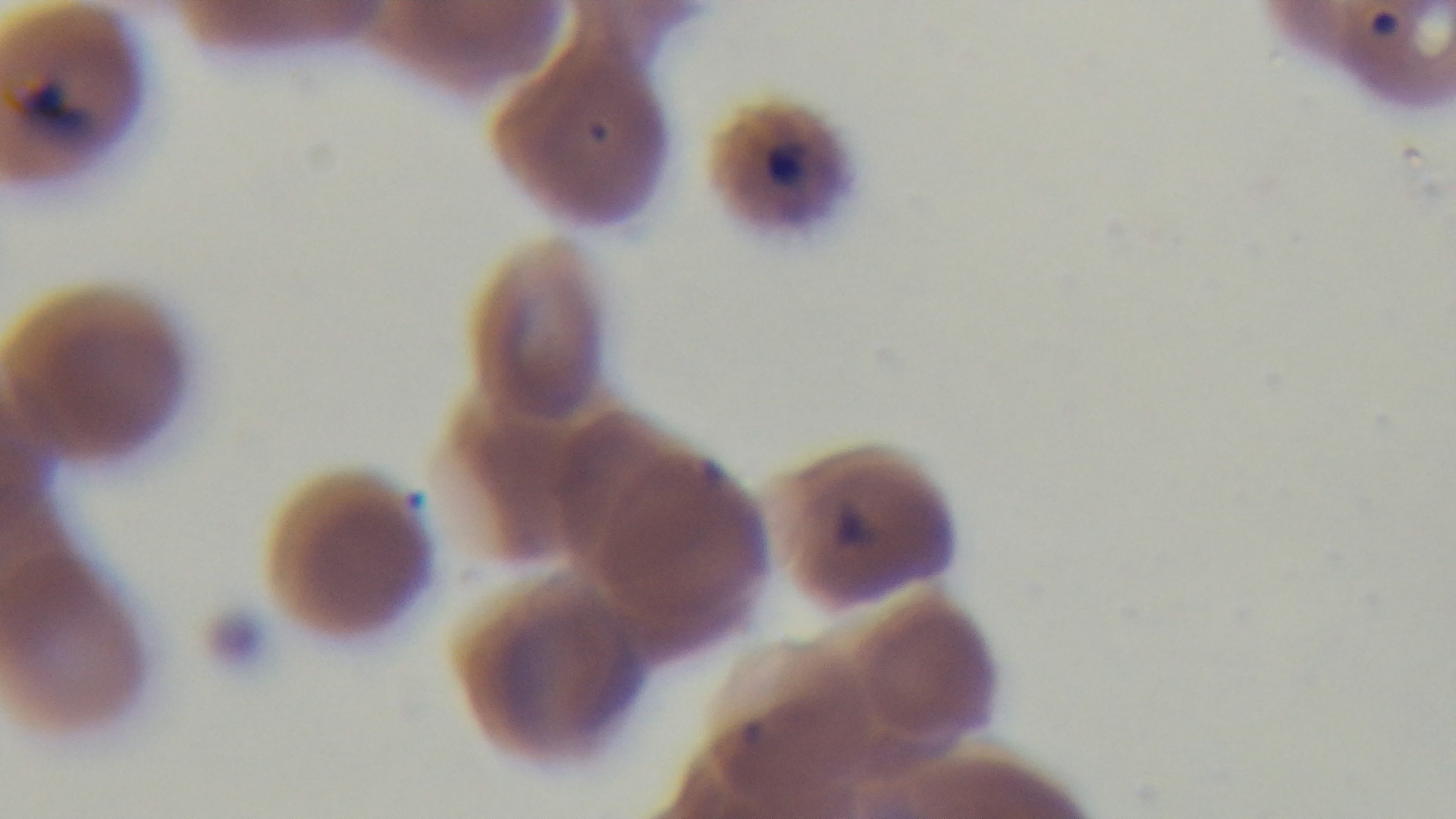
malaria_status: infected
modality: light microscopy
objective: 100x oil immersion
field_of_view: single
capture: mounted 4K digital camera
stain: Giemsa
preparation: thin